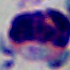

identification = white blood cell
magnification = 1000x
modality = micrograph